Assess the morphology of the erythrocytes.
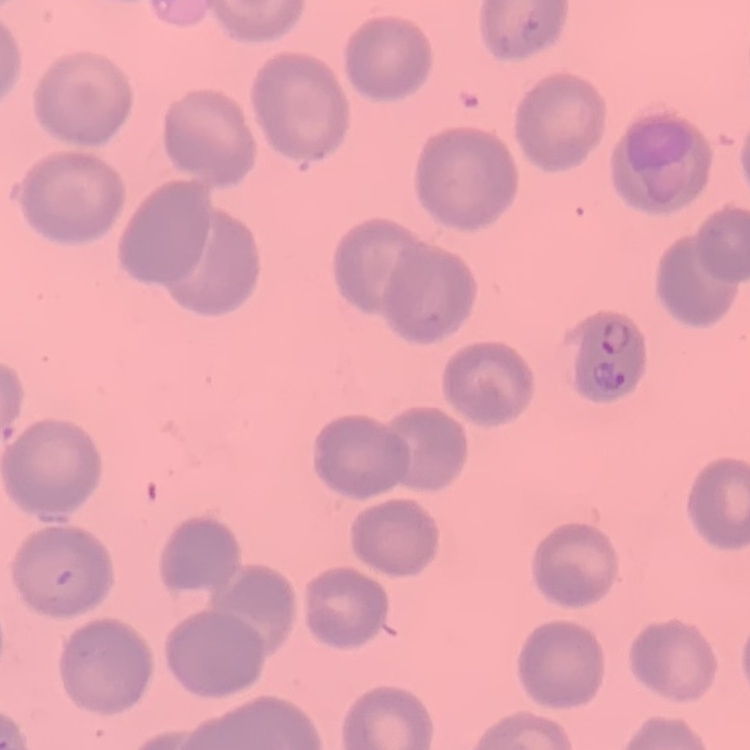

No rouleaux formation.

image type = square crop of a larger photomicrograph
preparation = thin blood smear
stain = Field's or Giemsa